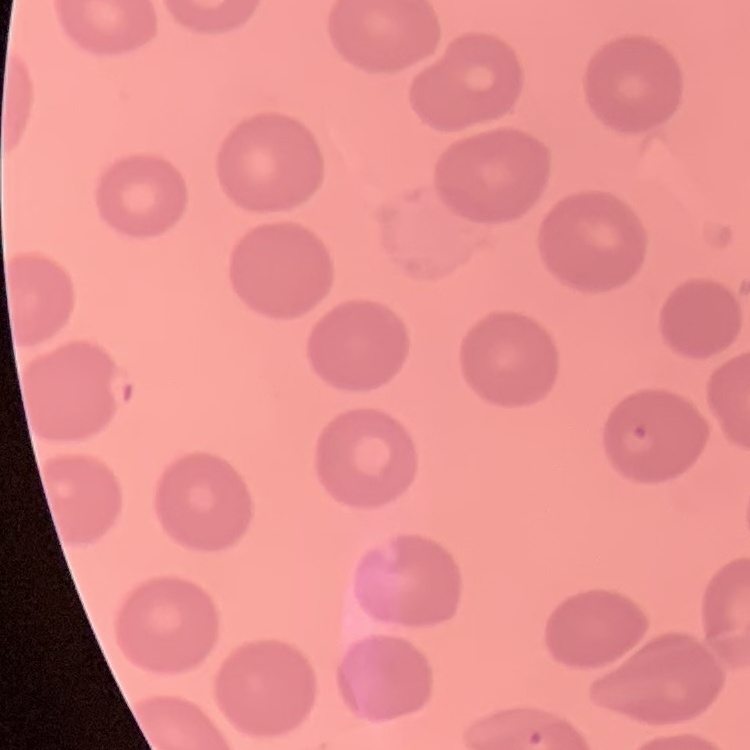

Summary:
  - Erythrocyte morphology: no rouleaux formation
  - Stain: Field's or Giemsa
  - Image type: square crop of a larger photomicrograph
  - Preparation: thin blood smear